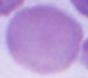

identification: erythrocyte
magnification: 1000x
modality: micrograph